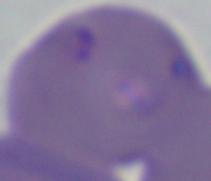

A Babesia parasite is seen. Captured at 1000x magnification. Micrograph.